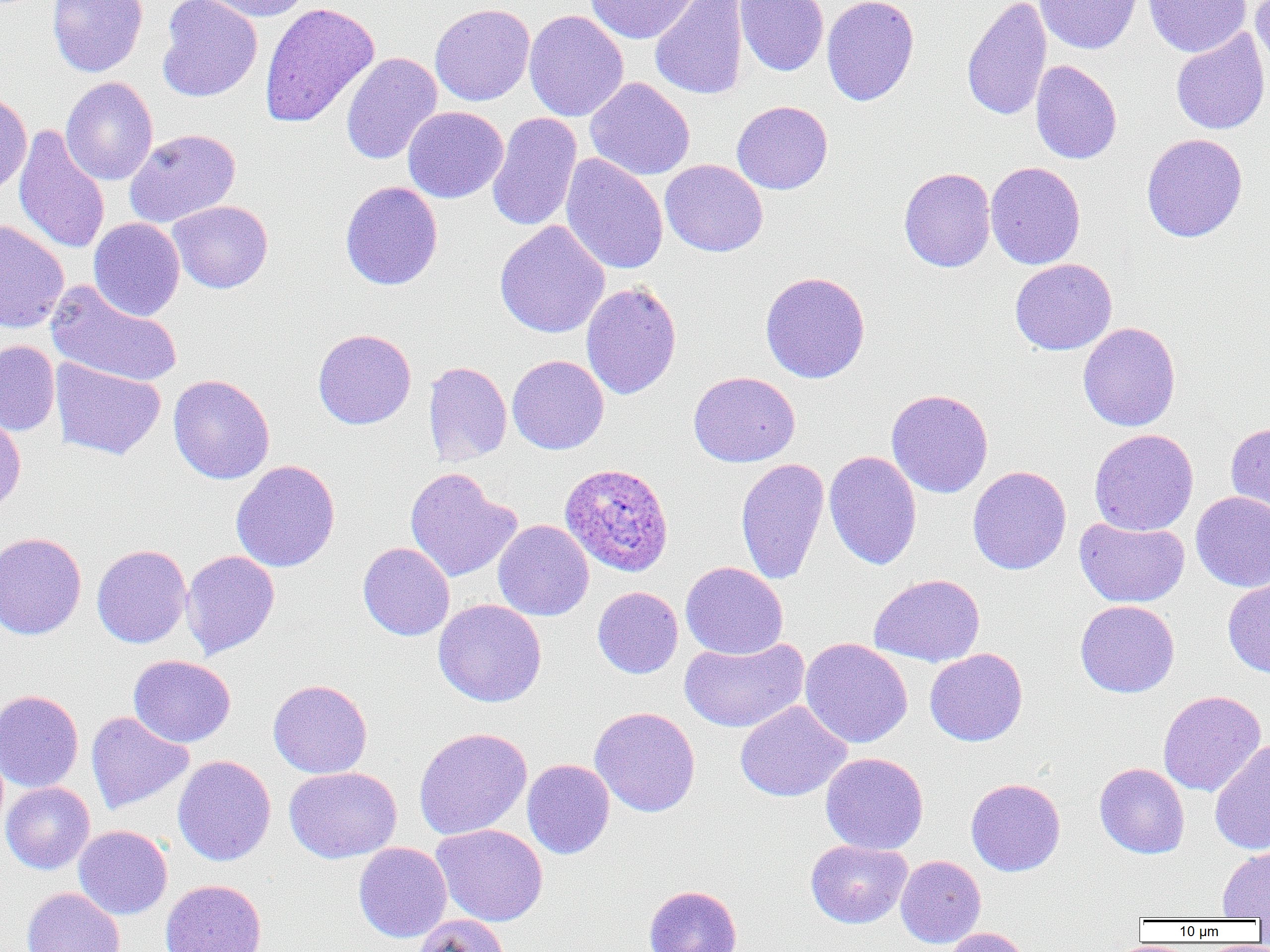
Summary:
  - Coordinate format: approximate bounding boxes as (x1, y1, x2, y2) in pixels
  - Uninfected red blood cell locations: (45, 0, 263, 80), (47, 0, 148, 78), (156, 0, 262, 102), (195, 0, 311, 22), (583, 0, 703, 45), (650, 0, 749, 100), (735, 0, 829, 76), (822, 0, 919, 106), (961, 0, 1052, 122), (1035, 0, 1142, 54), (1143, 0, 1251, 58), (1251, 0, 1270, 75), (259, 2, 380, 128), (430, 3, 536, 106), (524, 10, 629, 122), (1170, 28, 1270, 135), (341, 52, 442, 165), (1030, 60, 1122, 164), (60, 76, 158, 186), (585, 77, 695, 180), (0, 91, 32, 196), (732, 100, 833, 195), (402, 106, 509, 203), (487, 112, 582, 233), (14, 124, 110, 254), (124, 128, 240, 228), (1141, 133, 1248, 242), (561, 153, 668, 275), (660, 159, 768, 257), (985, 162, 1086, 269), (898, 167, 996, 272), (340, 181, 443, 290), (167, 200, 273, 294), (88, 218, 185, 320), (0, 220, 69, 335), (494, 220, 610, 339), (1010, 258, 1117, 355), (759, 271, 871, 383), (46, 281, 182, 388), (581, 282, 682, 399), (1078, 322, 1181, 432), (312, 328, 416, 429), (0, 340, 60, 435), (507, 354, 609, 455), (50, 358, 166, 460), (422, 361, 513, 466), (688, 371, 800, 467), (168, 374, 275, 484), (886, 389, 994, 498), (0, 412, 26, 518), (1225, 421, 1270, 523), (1089, 428, 1199, 536), (823, 450, 922, 570), (735, 457, 829, 585), (231, 460, 341, 572), (967, 465, 1072, 575), (404, 467, 521, 582), (1190, 491, 1270, 592), (1074, 517, 1189, 607), (493, 520, 594, 621), (0, 531, 88, 640), (357, 542, 455, 641), (91, 544, 191, 648), (181, 550, 280, 659), (680, 562, 789, 659), (869, 573, 985, 667), (1222, 577, 1270, 678), (592, 586, 683, 678), (433, 599, 547, 707), (1075, 599, 1180, 698), (680, 637, 809, 733), (800, 637, 913, 749), (924, 648, 1028, 746), (128, 655, 236, 747), (268, 679, 372, 779), (0, 689, 84, 793), (1158, 690, 1266, 796), (735, 700, 851, 802), (590, 706, 701, 818), (86, 710, 194, 814), (414, 727, 533, 840), (1210, 738, 1270, 856), (821, 752, 929, 855), (172, 755, 276, 866), (522, 759, 615, 859), (1094, 762, 1190, 859), (284, 766, 402, 863), (965, 777, 1066, 876), (1, 782, 95, 874), (432, 824, 549, 926), (74, 825, 172, 919), (805, 839, 912, 928), (353, 842, 452, 943), (1217, 845, 1270, 920), (896, 855, 986, 948), (160, 879, 267, 952), (644, 885, 742, 952), (22, 887, 125, 952), (413, 915, 510, 952), (940, 927, 1031, 952)
  - Plasmodium ovale-infected red blood cell locations: (560, 462, 674, 576)
  - Slide-level diagnosis: Plasmodium ovale
  - Image size: 1270×952 pixels
  - Field of view: single
  - Preparation: thin blood smear
  - Modality: light microscopy
  - Magnification: 1000x